Classify this cell by malaria status.
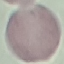
Uninfected.

preparation = thin blood smear
stain = Giemsa
capture = smartphone camera at the microscope eyepiece
image type = automatically extracted cell patch, resized to 64 × 64 pixels